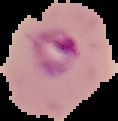
image type = segmented cell region with the area outside set to black
preparation = thin blood film
image size = 118×121 pixels
malaria status = parasitized